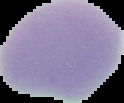
preparation = thin blood smear
image type = segmented cell region on a black background
image size = 124×103 pixels
result = no Plasmodium parasites seen